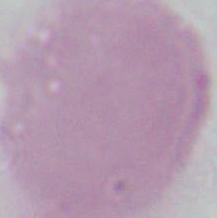
Summary:
  - Identification: erythrocyte
  - Magnification: 1000x
  - Modality: micrograph